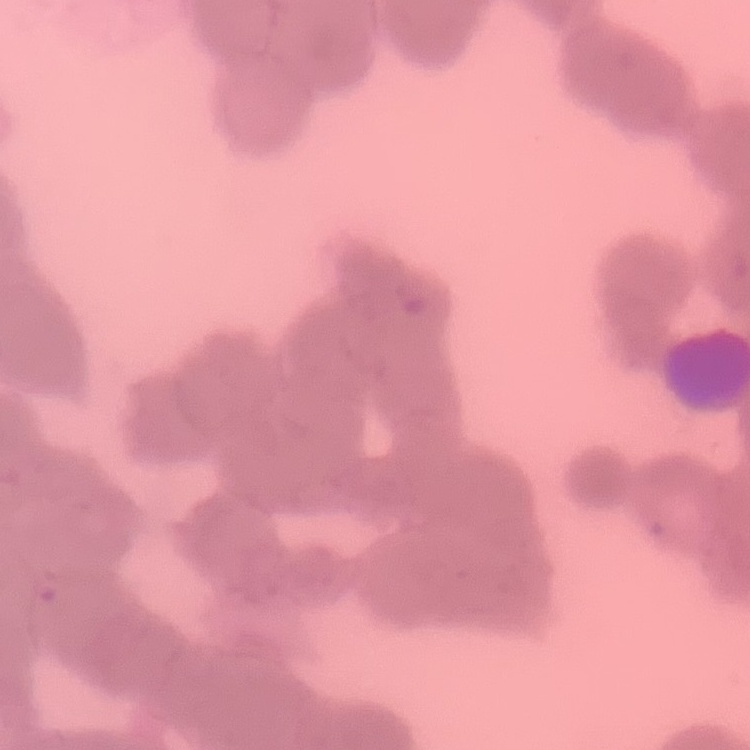

The erythrocytes exhibit rouleaux formation. Thin peripheral smear. Square crop of a larger photomicrograph. Stained with either Field's or Giemsa.